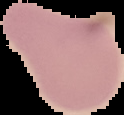

Segmented cell region on a black background. From a thin blood smear. Malaria status: uninfected. Image is 124×115 pixels.